Report the malaria status of this cell.
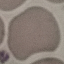
Uninfected.

Cell patch, automatically extracted from a larger field of view and resized to 64 × 64 pixels. Giemsa-stained preparation. Thin blood smear. Photographed with a smartphone camera at the microscope eyepiece.